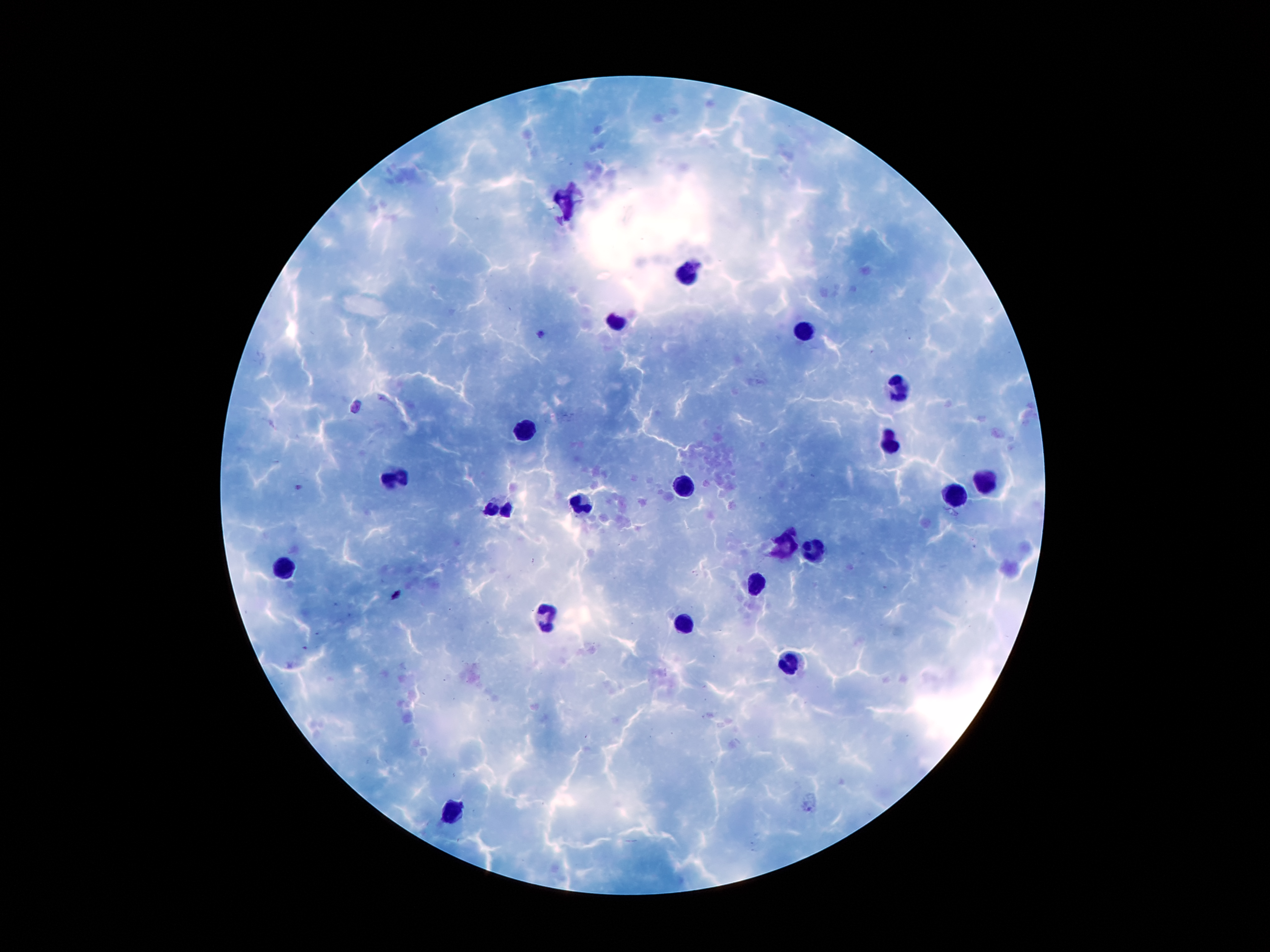
Approximate centers as {x, y} in pixels.
Summary:
  - Leukocyte locations: {689, 269}, {616, 322}, {899, 385}, {522, 429}, {891, 442}, {399, 477}, {985, 478}, {684, 485}, {957, 495}, {502, 506}, {581, 506}, {791, 549}, {815, 549}, {285, 569}, {756, 582}, {547, 614}, {684, 623}, {791, 665}, {451, 816}
  - Plasmodium parasite locations: {542, 333}, {301, 487}, {397, 594}
  - Magnification: 100x
  - Stain: Giemsa
  - Preparation: thick peripheral-blood smear
  - Patient malaria status: positive for Plasmodium falciparum
  - Capture: smartphone camera through the microscope eyepiece
  - Image size: 1270×952 pixels
  - Field of view: one from this slide